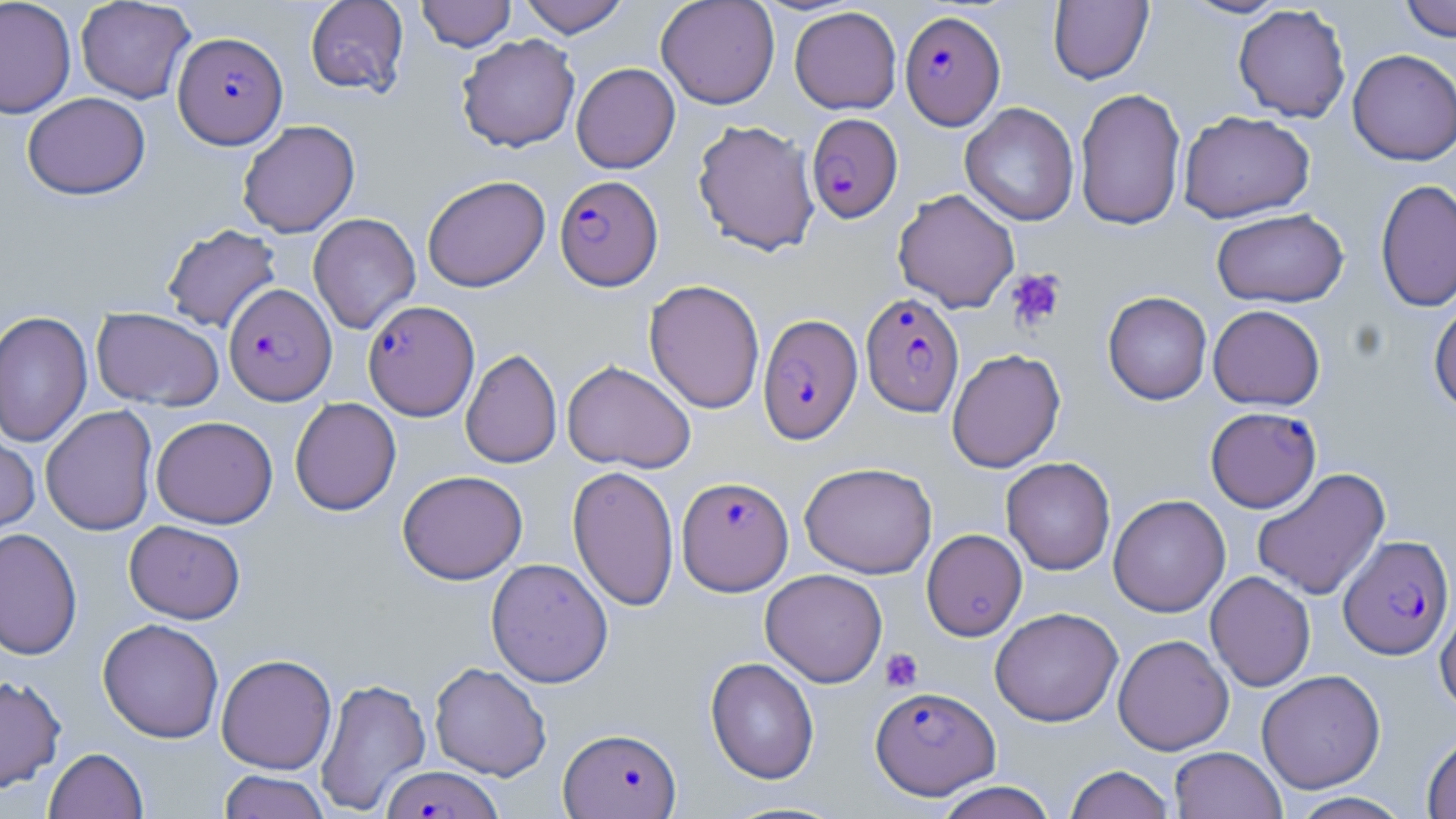
Summary:
  - Coordinate format: approximate bounding boxes as (x1, y1, x2, y2) in pixels
  - Platelet locations: (1005, 269, 1066, 331), (880, 648, 923, 692)
  - Uninfected red blood cell locations: (0, 0, 76, 118), (75, 0, 195, 103), (305, 0, 409, 96), (416, 0, 516, 52), (517, 0, 630, 37), (655, 0, 780, 109), (1179, 0, 1290, 19), (1398, 0, 1456, 41), (1048, 1, 1153, 85), (1233, 4, 1351, 122), (789, 6, 902, 114), (456, 33, 580, 153), (1347, 49, 1456, 166), (571, 62, 680, 174), (1074, 87, 1186, 230), (22, 92, 151, 199), (960, 103, 1079, 226), (1178, 110, 1315, 223), (693, 119, 820, 256), (237, 120, 360, 238), (422, 175, 550, 292), (1375, 179, 1456, 313), (893, 188, 1020, 312), (1211, 208, 1348, 307), (308, 213, 421, 334), (162, 223, 282, 333), (643, 279, 765, 414), (1102, 291, 1212, 405), (1429, 298, 1456, 417), (1208, 304, 1326, 411), (91, 307, 225, 410), (0, 310, 92, 448), (946, 348, 1066, 473), (460, 349, 562, 469), (562, 359, 697, 474), (290, 397, 401, 516), (40, 405, 158, 536), (151, 416, 278, 528), (0, 428, 40, 543), (1001, 457, 1116, 575), (799, 461, 938, 578), (567, 464, 679, 613), (1251, 467, 1391, 601), (397, 469, 528, 585), (1108, 494, 1231, 617), (124, 520, 245, 623), (0, 528, 83, 661), (921, 529, 1027, 641), (485, 557, 613, 688), (760, 568, 888, 687), (1205, 571, 1315, 692), (1435, 595, 1456, 716), (989, 607, 1123, 727), (97, 618, 224, 743), (1113, 634, 1234, 755), (216, 653, 337, 774), (705, 656, 820, 784), (429, 662, 552, 780), (1256, 669, 1386, 793), (0, 674, 66, 793), (315, 677, 431, 816), (1422, 732, 1456, 819), (1169, 746, 1285, 819), (44, 747, 148, 819), (1063, 764, 1175, 819), (218, 770, 330, 818), (933, 781, 1059, 819), (1288, 792, 1412, 819)
  - Plasmodium falciparum-infected red blood cell locations: (900, 9, 1005, 130), (173, 31, 288, 148), (806, 113, 903, 223), (554, 174, 663, 291), (223, 283, 337, 405), (860, 292, 964, 417), (363, 300, 480, 420), (757, 313, 863, 445), (1205, 406, 1321, 512), (677, 476, 793, 596), (1338, 534, 1454, 659), (871, 685, 1000, 799), (559, 727, 682, 818), (381, 765, 504, 819)
  - Slide-level diagnosis: Plasmodium falciparum
  - Image size: 1456×819 pixels
  - Preparation: thin blood film
  - Stain: May-Grünwald-Giemsa
  - Magnification: 1000x
  - Modality: light microscopy
  - Field of view: single